Give the extent of all Plasmodium malariae-infected red blood cells.
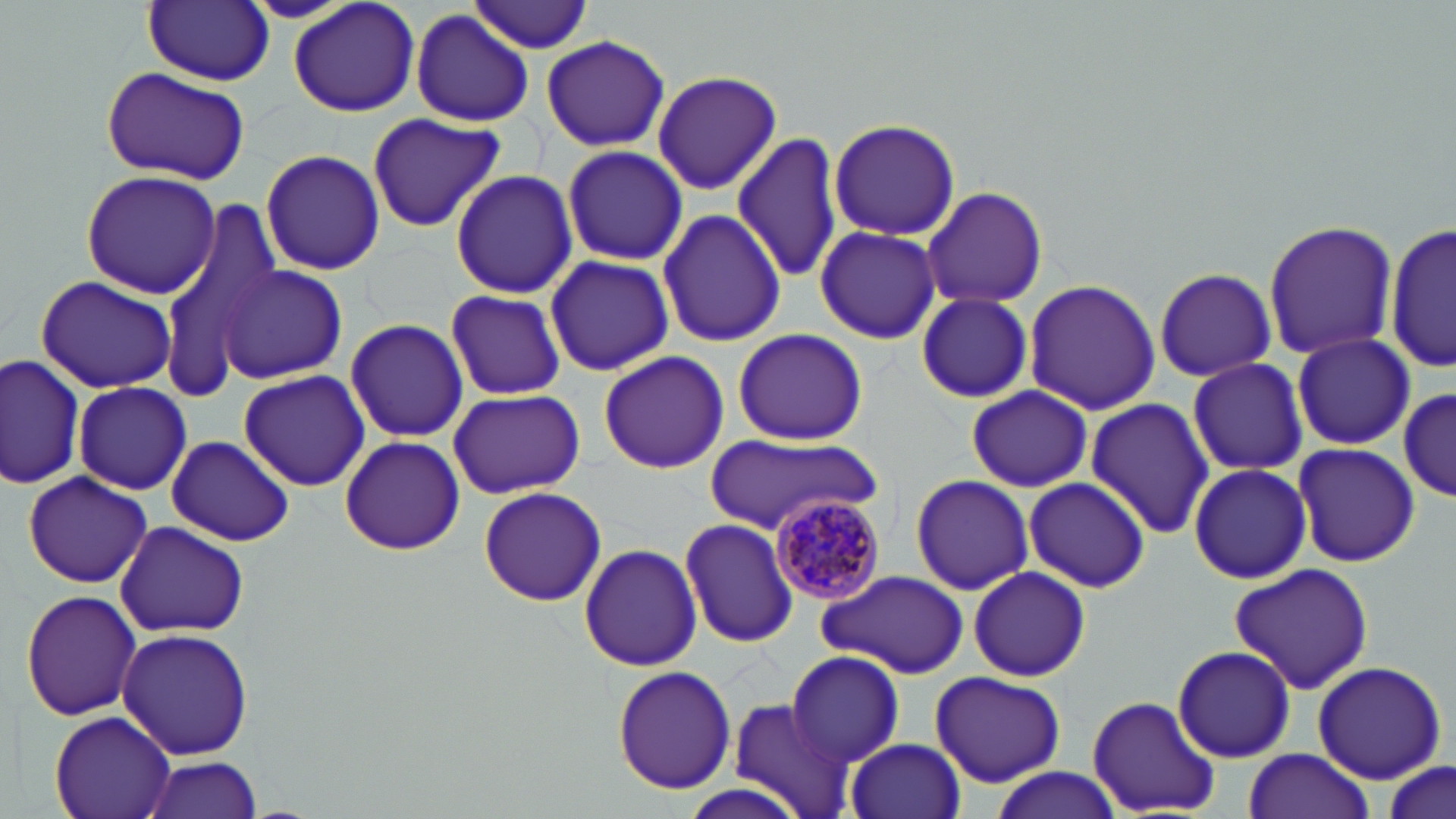
Approximate bounding boxes as named x1/y1/x2/y2 corners in pixels.
Plasmodium malariae-infected red blood cells: (x1=768, y1=493, x2=888, y2=607).

Summary:
  - Uninfected red blood cell locations: (x1=239, y1=0, x2=359, y2=24), (x1=287, y1=0, x2=422, y2=118), (x1=144, y1=1, x2=272, y2=85), (x1=466, y1=2, x2=592, y2=54), (x1=410, y1=11, x2=534, y2=127), (x1=540, y1=34, x2=671, y2=153), (x1=99, y1=65, x2=251, y2=182), (x1=650, y1=69, x2=781, y2=195), (x1=365, y1=111, x2=507, y2=232), (x1=827, y1=118, x2=961, y2=242), (x1=733, y1=131, x2=843, y2=283), (x1=560, y1=144, x2=689, y2=267), (x1=260, y1=148, x2=384, y2=277), (x1=81, y1=169, x2=223, y2=299), (x1=449, y1=169, x2=579, y2=299), (x1=921, y1=185, x2=1048, y2=310), (x1=656, y1=206, x2=786, y2=350), (x1=153, y1=208, x2=286, y2=386), (x1=1263, y1=219, x2=1398, y2=361), (x1=1387, y1=222, x2=1454, y2=373), (x1=816, y1=227, x2=942, y2=344), (x1=544, y1=252, x2=673, y2=378), (x1=218, y1=266, x2=348, y2=386), (x1=1153, y1=266, x2=1276, y2=384), (x1=33, y1=275, x2=179, y2=394), (x1=1023, y1=278, x2=1161, y2=415), (x1=445, y1=288, x2=567, y2=401), (x1=914, y1=293, x2=1033, y2=402), (x1=344, y1=317, x2=470, y2=442), (x1=733, y1=327, x2=868, y2=447), (x1=1290, y1=333, x2=1415, y2=451), (x1=597, y1=350, x2=729, y2=475), (x1=2, y1=352, x2=86, y2=491), (x1=1188, y1=358, x2=1310, y2=475), (x1=237, y1=370, x2=370, y2=491), (x1=73, y1=381, x2=191, y2=495), (x1=966, y1=384, x2=1093, y2=492), (x1=446, y1=388, x2=585, y2=499), (x1=1399, y1=389, x2=1456, y2=502), (x1=1085, y1=396, x2=1214, y2=541), (x1=339, y1=434, x2=466, y2=557), (x1=164, y1=435, x2=296, y2=546), (x1=705, y1=435, x2=880, y2=535), (x1=1289, y1=443, x2=1420, y2=569), (x1=1186, y1=462, x2=1313, y2=585), (x1=21, y1=471, x2=154, y2=588), (x1=910, y1=473, x2=1033, y2=595), (x1=1024, y1=476, x2=1150, y2=593), (x1=994, y1=485, x2=1129, y2=668), (x1=477, y1=486, x2=606, y2=607), (x1=679, y1=517, x2=800, y2=648), (x1=112, y1=521, x2=249, y2=638), (x1=579, y1=541, x2=701, y2=673), (x1=1227, y1=563, x2=1375, y2=693), (x1=967, y1=565, x2=1090, y2=681), (x1=815, y1=568, x2=968, y2=678), (x1=19, y1=589, x2=143, y2=723), (x1=116, y1=628, x2=256, y2=760), (x1=1171, y1=643, x2=1297, y2=763), (x1=786, y1=650, x2=906, y2=765), (x1=1312, y1=660, x2=1447, y2=784), (x1=612, y1=664, x2=737, y2=794), (x1=929, y1=669, x2=1065, y2=787), (x1=1087, y1=695, x2=1220, y2=815), (x1=728, y1=697, x2=851, y2=817), (x1=50, y1=712, x2=175, y2=819), (x1=846, y1=736, x2=966, y2=819), (x1=1242, y1=748, x2=1377, y2=819), (x1=140, y1=755, x2=264, y2=818), (x1=1378, y1=758, x2=1454, y2=819), (x1=987, y1=767, x2=1123, y2=819)
  - Slide-level diagnosis: Plasmodium malariae
  - Image size: 1456×819 pixels
  - Modality: optical microscopy
  - Field of view: single
  - Magnification: 1000x
  - Stain: May-Grünwald-Giemsa
  - Preparation: thin blood smear